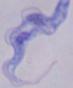
Summary:
  - Modality: photomicrograph
  - Identification: trypanosome
  - Magnification: 1000x